Assess for parasitized red blood cells.
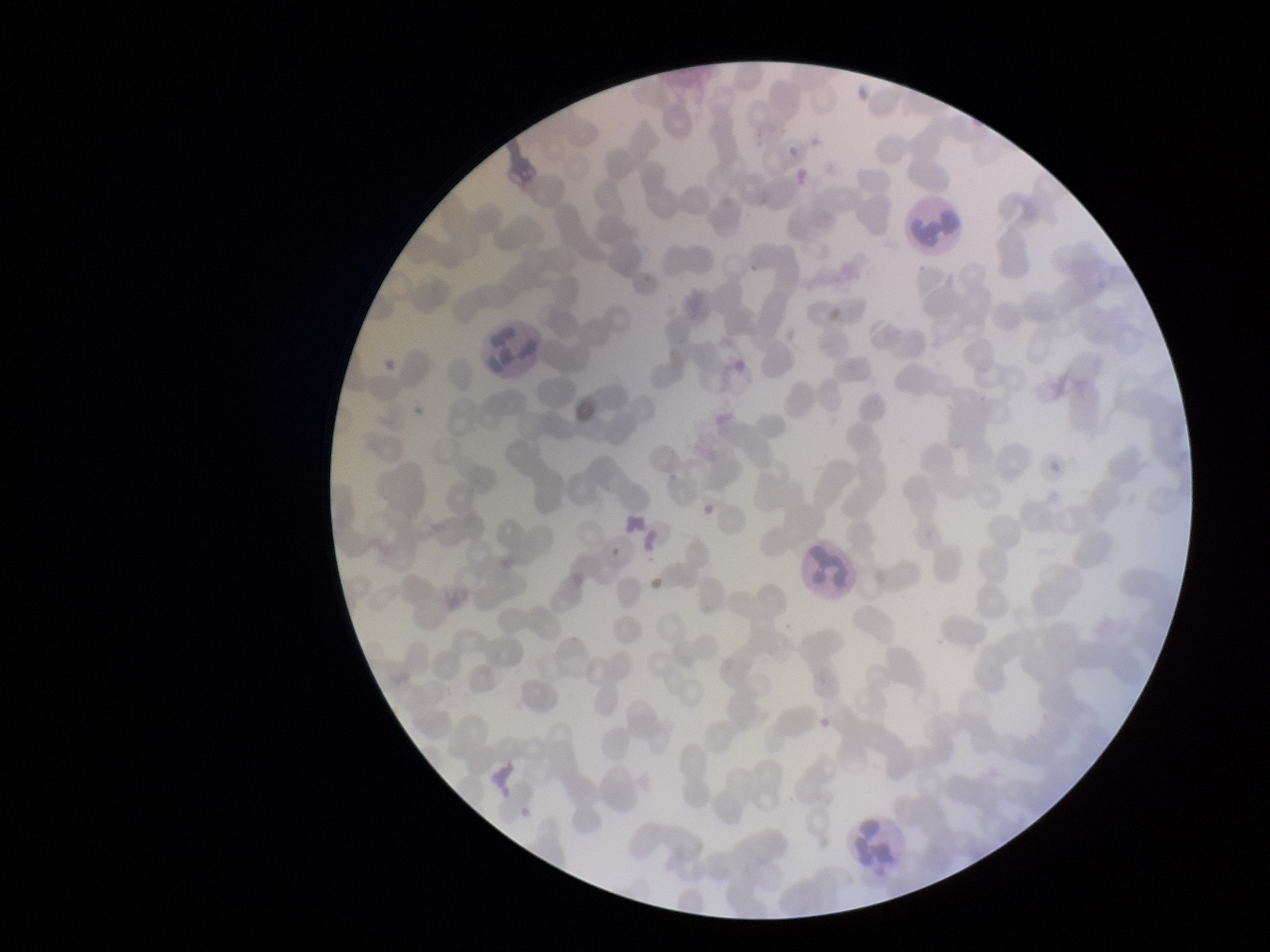
None detected.

capture = smartphone photograph through the microscope eyepiece
red blood cell count = 253
image size = 1270×952 pixels
field of view = single
preparation = thin smear
parasitized red blood cell count = 0
patient malaria status = negative
stain = Giemsa